Report the malaria status.
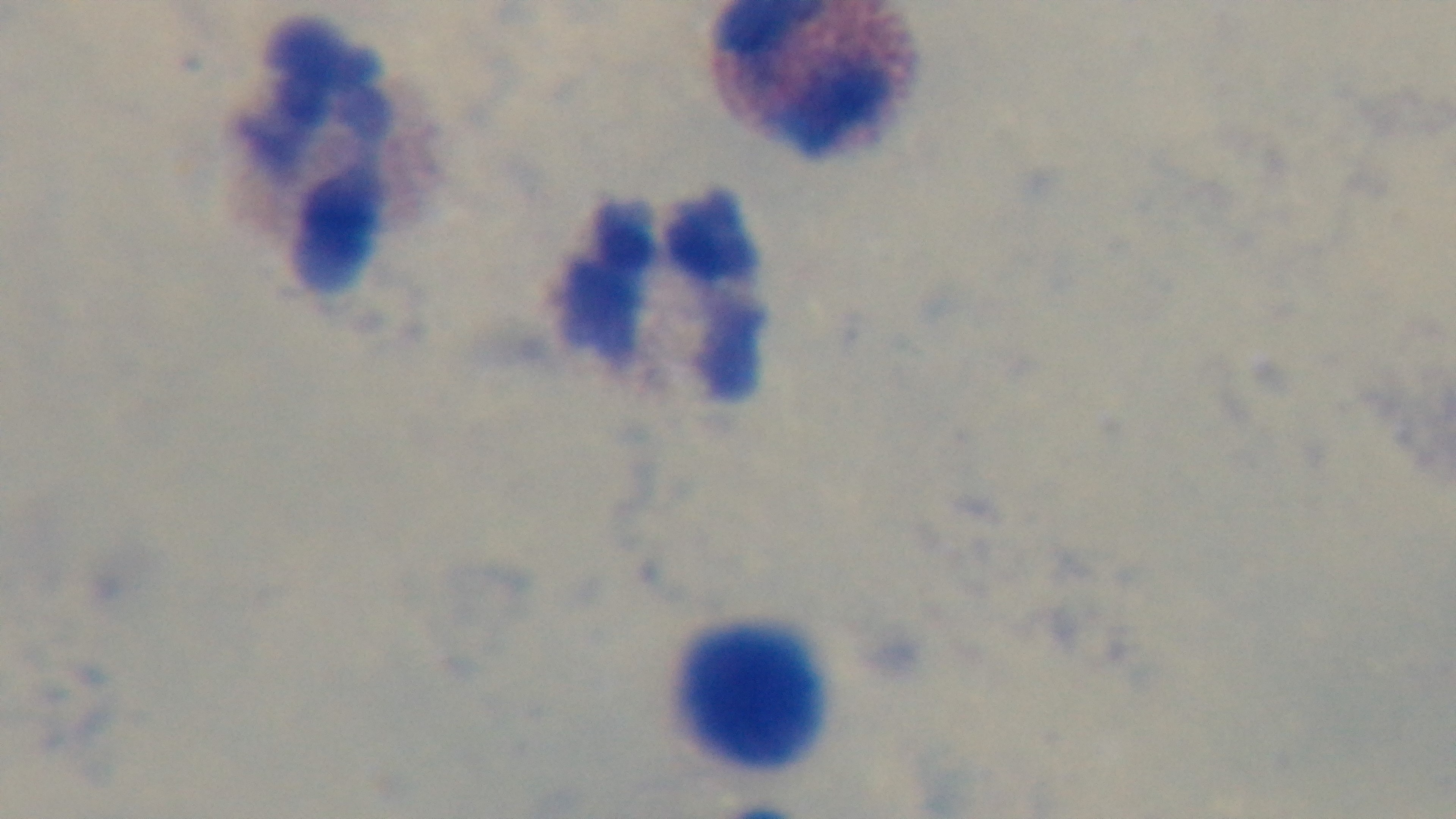

Uninfected.

Preparation: thick smear. Single field of view. Oil-immersion objective, 100x. Captured with a mounted 4K digital camera. Giemsa-stained. Photomicrograph.